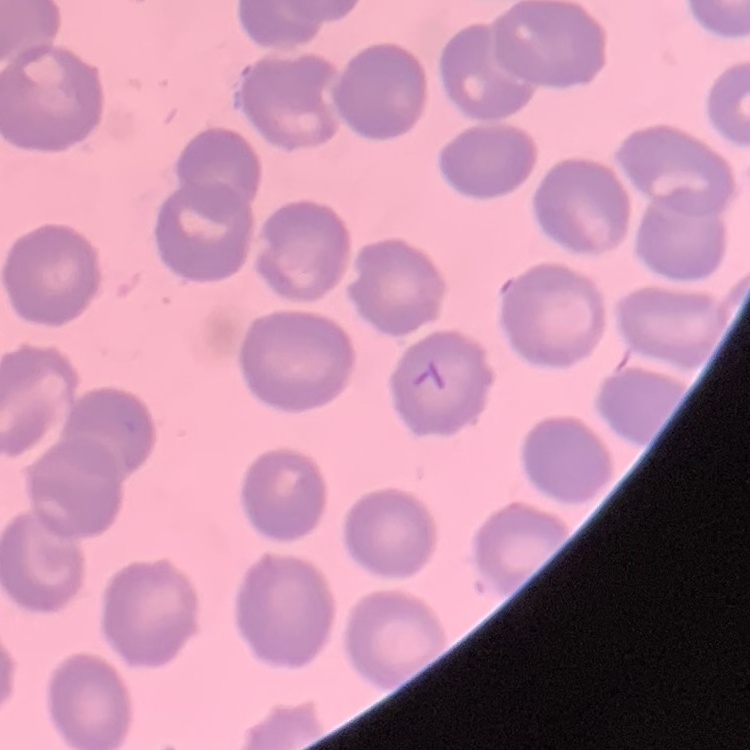
The red blood cells show no rouleaux formation. Stained with either Field's or Giemsa. Thin peripheral smear. Square crop of a larger photomicrograph.